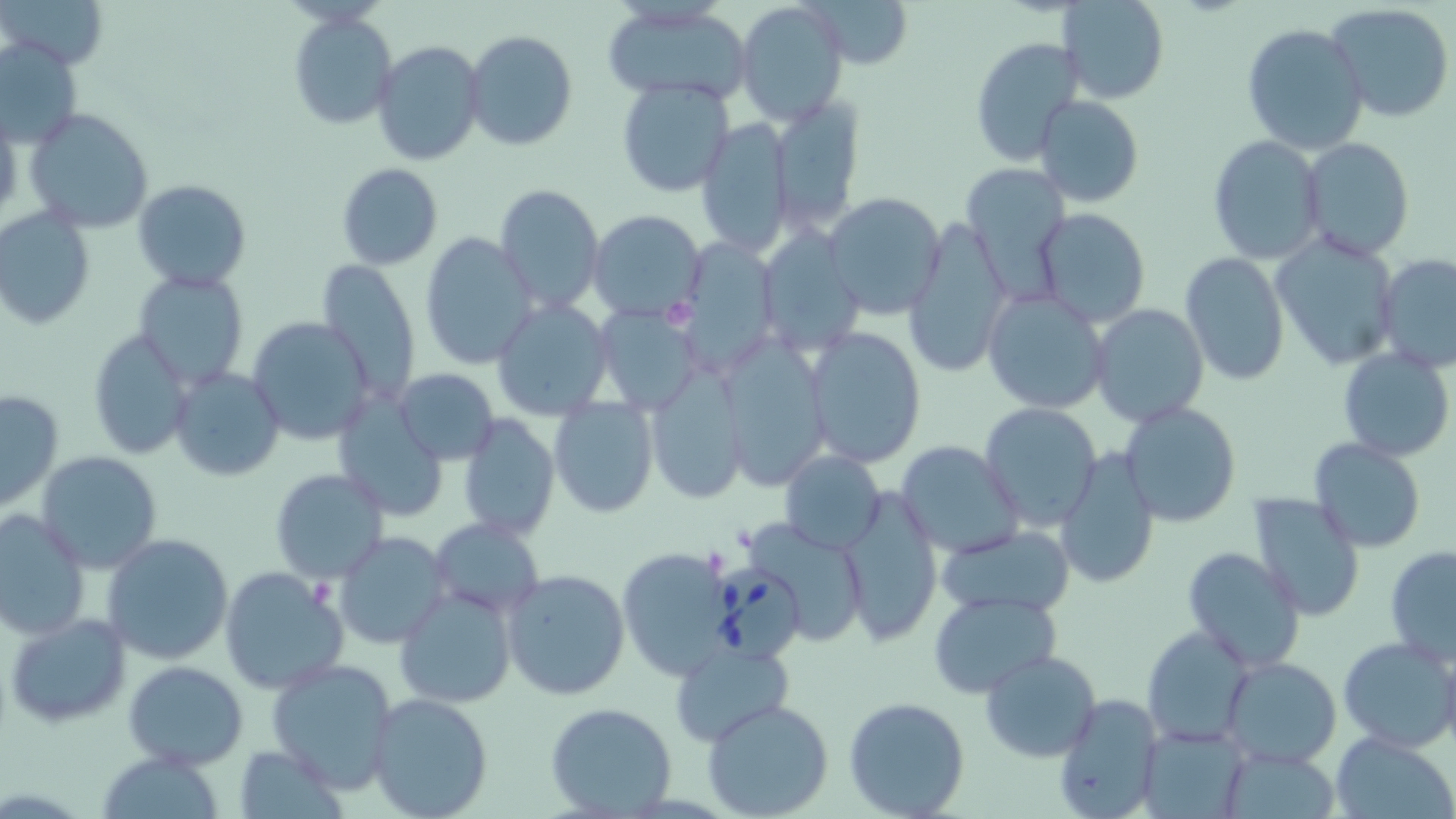
Summary:
  - Coordinate format: approximate bounding boxes as named x1/y1/x2/y2 corners in pixels
  - Uninfected red blood cell locations: (x1=3, y1=0, x2=107, y2=69), (x1=811, y1=0, x2=916, y2=69), (x1=1058, y1=0, x2=1169, y2=104), (x1=735, y1=2, x2=849, y2=127), (x1=602, y1=4, x2=750, y2=105), (x1=1327, y1=4, x2=1455, y2=122), (x1=288, y1=12, x2=397, y2=129), (x1=1240, y1=22, x2=1370, y2=155), (x1=464, y1=30, x2=577, y2=151), (x1=0, y1=37, x2=83, y2=151), (x1=970, y1=37, x2=1085, y2=167), (x1=372, y1=40, x2=486, y2=167), (x1=616, y1=78, x2=736, y2=197), (x1=1032, y1=95, x2=1144, y2=207), (x1=769, y1=96, x2=865, y2=233), (x1=0, y1=104, x2=22, y2=224), (x1=25, y1=106, x2=153, y2=232), (x1=695, y1=117, x2=794, y2=260), (x1=1208, y1=134, x2=1325, y2=265), (x1=1300, y1=137, x2=1415, y2=259), (x1=336, y1=162, x2=442, y2=270), (x1=962, y1=162, x2=1071, y2=293), (x1=133, y1=178, x2=251, y2=291), (x1=933, y1=181, x2=1049, y2=343), (x1=495, y1=183, x2=606, y2=312), (x1=823, y1=191, x2=947, y2=318), (x1=1036, y1=208, x2=1150, y2=328), (x1=0, y1=209, x2=95, y2=330), (x1=588, y1=211, x2=707, y2=322), (x1=906, y1=213, x2=1014, y2=379), (x1=757, y1=227, x2=866, y2=353), (x1=1271, y1=230, x2=1402, y2=371), (x1=421, y1=232, x2=540, y2=371), (x1=673, y1=237, x2=778, y2=375), (x1=1179, y1=252, x2=1291, y2=386), (x1=1376, y1=253, x2=1456, y2=371), (x1=319, y1=258, x2=423, y2=402), (x1=136, y1=267, x2=248, y2=387), (x1=981, y1=288, x2=1111, y2=416), (x1=491, y1=299, x2=615, y2=422), (x1=594, y1=303, x2=703, y2=416), (x1=1089, y1=304, x2=1212, y2=427), (x1=246, y1=315, x2=375, y2=446), (x1=805, y1=327, x2=927, y2=468), (x1=86, y1=328, x2=195, y2=459), (x1=717, y1=336, x2=829, y2=488), (x1=1338, y1=347, x2=1454, y2=462), (x1=646, y1=361, x2=750, y2=504), (x1=170, y1=367, x2=285, y2=480), (x1=393, y1=368, x2=499, y2=463), (x1=0, y1=389, x2=64, y2=512), (x1=331, y1=392, x2=450, y2=523), (x1=550, y1=397, x2=660, y2=518), (x1=1119, y1=400, x2=1242, y2=526), (x1=979, y1=403, x2=1103, y2=531), (x1=458, y1=411, x2=560, y2=541), (x1=1307, y1=438, x2=1430, y2=554), (x1=897, y1=440, x2=1023, y2=559), (x1=1054, y1=447, x2=1161, y2=591), (x1=35, y1=450, x2=163, y2=573), (x1=778, y1=451, x2=887, y2=554), (x1=270, y1=469, x2=388, y2=584), (x1=839, y1=491, x2=943, y2=645), (x1=1247, y1=492, x2=1367, y2=624), (x1=0, y1=510, x2=92, y2=641), (x1=430, y1=516, x2=544, y2=617), (x1=739, y1=520, x2=872, y2=648), (x1=937, y1=524, x2=1073, y2=617), (x1=334, y1=531, x2=451, y2=651), (x1=101, y1=532, x2=234, y2=667), (x1=1384, y1=544, x2=1456, y2=667), (x1=1183, y1=545, x2=1306, y2=671), (x1=617, y1=546, x2=736, y2=679), (x1=218, y1=566, x2=349, y2=696), (x1=502, y1=567, x2=632, y2=702), (x1=394, y1=585, x2=517, y2=710), (x1=928, y1=589, x2=1062, y2=696), (x1=5, y1=612, x2=132, y2=729), (x1=1140, y1=624, x2=1254, y2=747), (x1=1337, y1=636, x2=1456, y2=752), (x1=668, y1=639, x2=795, y2=747), (x1=979, y1=650, x2=1101, y2=762), (x1=1222, y1=655, x2=1342, y2=768), (x1=267, y1=657, x2=400, y2=790), (x1=123, y1=660, x2=248, y2=769), (x1=365, y1=693, x2=494, y2=819), (x1=1051, y1=693, x2=1164, y2=819), (x1=842, y1=697, x2=971, y2=819), (x1=702, y1=699, x2=835, y2=819), (x1=544, y1=702, x2=678, y2=819), (x1=1138, y1=723, x2=1249, y2=818), (x1=1331, y1=731, x2=1454, y2=818), (x1=235, y1=744, x2=346, y2=817), (x1=1220, y1=748, x2=1340, y2=816), (x1=99, y1=749, x2=227, y2=817)
  - Babesia divergens-infected red blood cell locations: (x1=708, y1=564, x2=807, y2=664)
  - Slide-level diagnosis: Babesia divergens
  - Preparation: thin blood film
  - Modality: optical microscopy
  - Field of view: single
  - Stain: May-Grünwald-Giemsa
  - Magnification: 1000x
  - Image size: 1456×819 pixels